Outline each Plasmodium ovale-infected red blood cell.
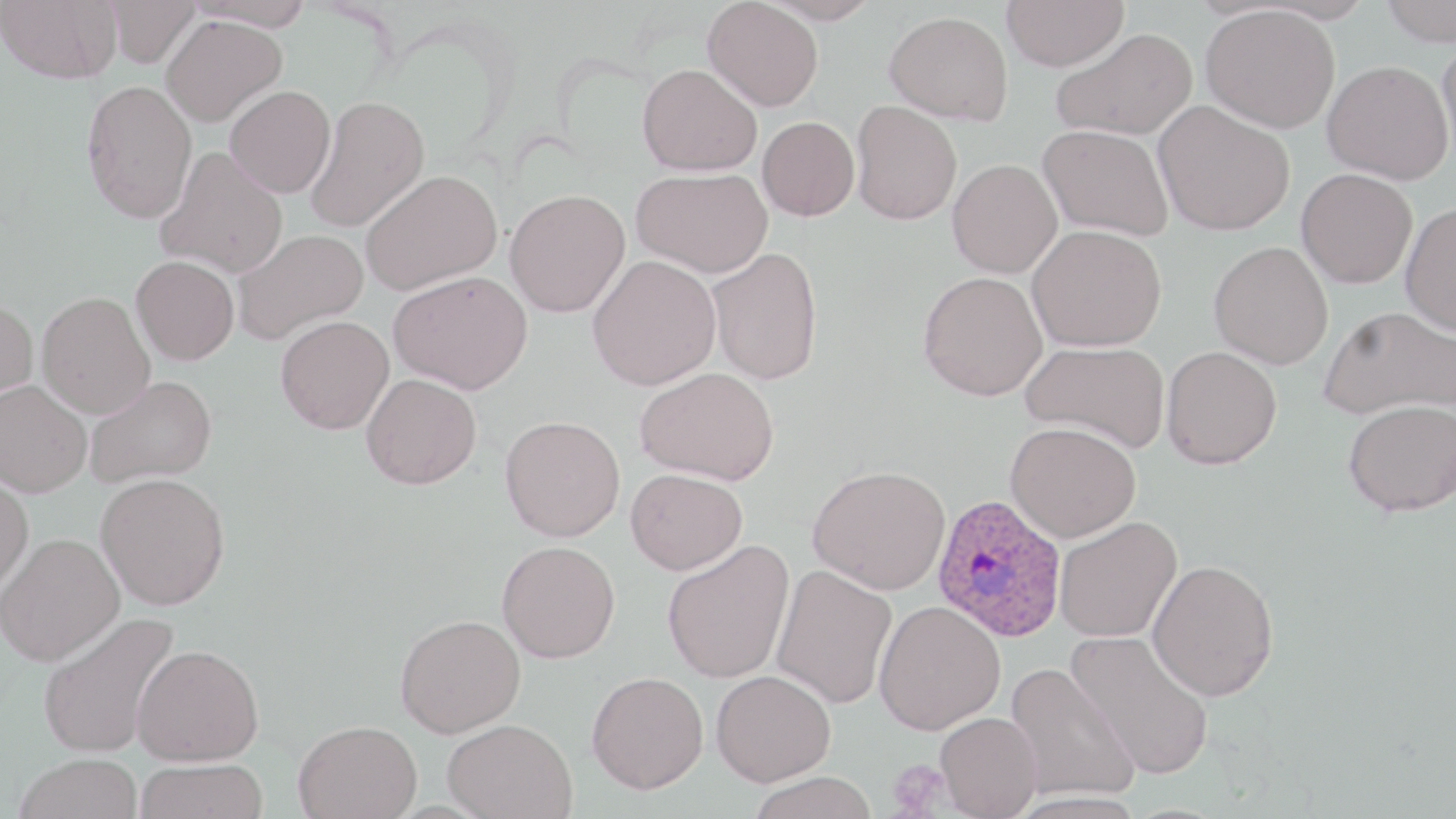

Approximate bounding boxes as named x1/y1/x2/y2 corners in pixels.
Plasmodium ovale-infected red blood cells: (x1=931, y1=494, x2=1067, y2=643).

{
  "slide_level_diagnosis": "Plasmodium ovale",
  "field_of_view": "one of a larger specimen",
  "magnification": "1000x",
  "uninfected_red_blood_cell_locations": "approximate bounding boxes as named x1/y1/x2/y2 corners in pixels: (x1=0, y1=0, x2=122, y2=84), (x1=104, y1=0, x2=201, y2=67), (x1=185, y1=0, x2=315, y2=31), (x1=703, y1=0, x2=824, y2=111), (x1=759, y1=0, x2=881, y2=25), (x1=1002, y1=0, x2=1129, y2=71), (x1=1380, y1=0, x2=1456, y2=46), (x1=1201, y1=5, x2=1340, y2=133), (x1=884, y1=11, x2=1013, y2=125), (x1=160, y1=14, x2=287, y2=126), (x1=1051, y1=27, x2=1196, y2=140), (x1=1436, y1=37, x2=1456, y2=170), (x1=1323, y1=60, x2=1454, y2=185), (x1=638, y1=63, x2=762, y2=176), (x1=80, y1=79, x2=197, y2=224), (x1=225, y1=85, x2=336, y2=198), (x1=304, y1=95, x2=429, y2=233), (x1=851, y1=100, x2=963, y2=225), (x1=1154, y1=101, x2=1295, y2=235), (x1=757, y1=116, x2=859, y2=221), (x1=1039, y1=124, x2=1173, y2=240), (x1=156, y1=146, x2=288, y2=279), (x1=948, y1=159, x2=1062, y2=278), (x1=631, y1=168, x2=773, y2=278), (x1=1296, y1=168, x2=1417, y2=288), (x1=360, y1=170, x2=502, y2=296), (x1=505, y1=188, x2=630, y2=317), (x1=1401, y1=201, x2=1456, y2=336), (x1=1027, y1=224, x2=1167, y2=352), (x1=232, y1=229, x2=368, y2=345), (x1=1208, y1=241, x2=1333, y2=369), (x1=706, y1=246, x2=824, y2=385), (x1=131, y1=255, x2=239, y2=365), (x1=587, y1=255, x2=722, y2=391), (x1=388, y1=270, x2=533, y2=394), (x1=917, y1=271, x2=1048, y2=402), (x1=36, y1=291, x2=155, y2=418), (x1=0, y1=297, x2=39, y2=404), (x1=1318, y1=306, x2=1456, y2=421), (x1=275, y1=315, x2=394, y2=434), (x1=1020, y1=340, x2=1170, y2=452), (x1=1161, y1=346, x2=1282, y2=470), (x1=635, y1=366, x2=780, y2=485), (x1=361, y1=373, x2=482, y2=490), (x1=84, y1=375, x2=217, y2=488), (x1=1, y1=380, x2=92, y2=497), (x1=1343, y1=399, x2=1456, y2=516), (x1=500, y1=414, x2=625, y2=542), (x1=1005, y1=422, x2=1141, y2=542), (x1=808, y1=465, x2=951, y2=595), (x1=625, y1=468, x2=747, y2=575), (x1=0, y1=472, x2=34, y2=596), (x1=95, y1=472, x2=230, y2=610), (x1=1054, y1=515, x2=1182, y2=643), (x1=0, y1=532, x2=124, y2=666), (x1=662, y1=539, x2=794, y2=684), (x1=497, y1=540, x2=620, y2=663), (x1=1147, y1=559, x2=1280, y2=701), (x1=771, y1=563, x2=897, y2=708), (x1=874, y1=600, x2=1005, y2=735), (x1=37, y1=611, x2=181, y2=759), (x1=395, y1=614, x2=526, y2=737), (x1=1066, y1=630, x2=1215, y2=780), (x1=132, y1=644, x2=264, y2=765), (x1=1004, y1=663, x2=1140, y2=804), (x1=711, y1=670, x2=836, y2=786), (x1=587, y1=672, x2=708, y2=794), (x1=935, y1=711, x2=1043, y2=818), (x1=442, y1=718, x2=577, y2=819), (x1=294, y1=719, x2=422, y2=819), (x1=13, y1=753, x2=143, y2=818), (x1=135, y1=758, x2=268, y2=819), (x1=746, y1=771, x2=880, y2=819), (x1=1008, y1=791, x2=1147, y2=818)",
  "modality": "optical microscopy",
  "preparation": "thin blood film",
  "platelet_locations": "approximate bounding boxes as named x1/y1/x2/y2 corners in pixels: (x1=886, y1=758, x2=952, y2=816)",
  "stain": "May-Grünwald-Giemsa",
  "image_size": "1456×819 pixels"
}